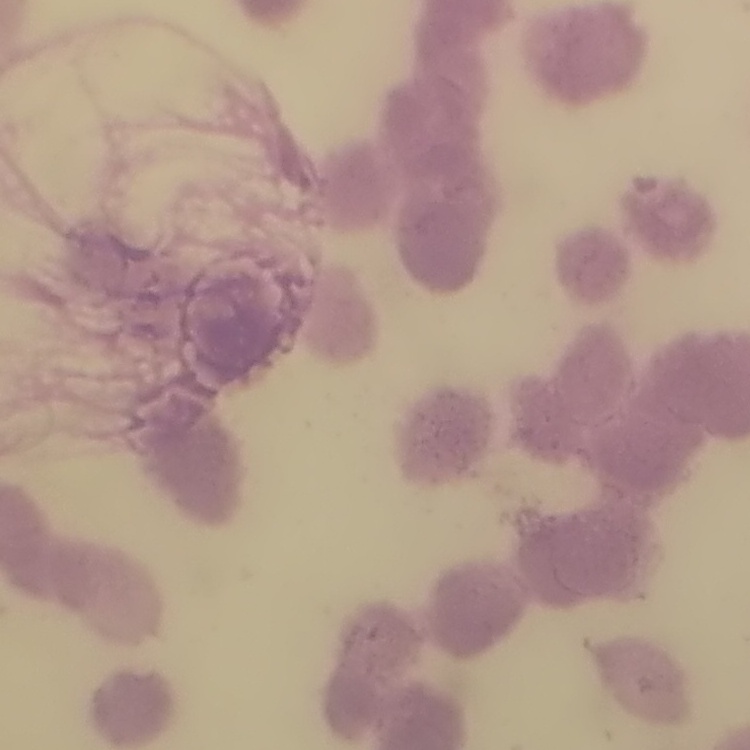 The red blood cells exhibit rouleaux formation. Thin blood smear. Field's or Giemsa stain. One tile cut from a larger photomicrograph.